Report the malaria status of this cell.
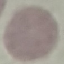

Uninfected.

Summary:
  - Image type: automatically extracted cell patch, resized to 64 × 64 pixels
  - Stain: Giemsa
  - Capture: smartphone through the microscope eyepiece
  - Preparation: thin blood smear